State which parasite is depicted.
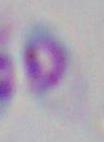

This is Toxoplasma gondii.

Summary:
  - Magnification: 1000x
  - Modality: photomicrograph